State which cell type is depicted.
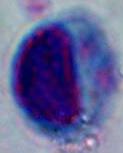
A leukocyte.

Photomicrograph. 1000x magnification.